Give a bounding box for every artifact (platelet-like body, stain precipitate, or debris).
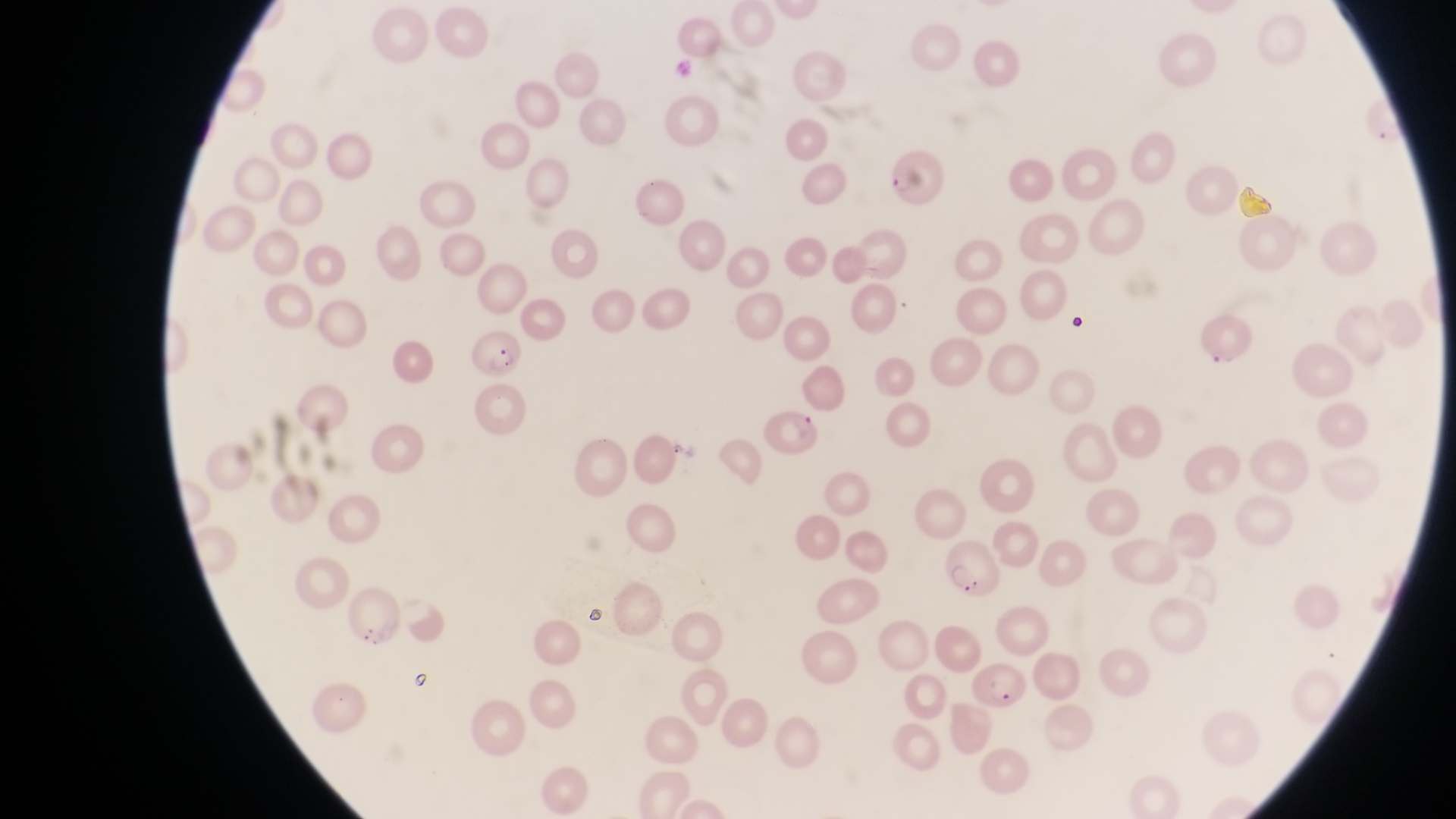
Approximate bounding boxes as [left, top, right, bottom] in pixels.
Artifacts (platelet-like body, stain precipitate, or debris): [1237, 179, 1280, 231], [1068, 312, 1091, 336], [582, 602, 606, 626], [409, 668, 441, 695].

magnification = 1000x
trophozoite locations = approximate bounding boxes as [left, top, right, bottom] in pixels: [667, 435, 694, 465]
parasitised red blood cell locations = approximate bounding boxes as [left, top, right, bottom] in pixels: [888, 151, 951, 212], [1199, 309, 1252, 370], [468, 330, 524, 379], [767, 404, 819, 453], [948, 544, 998, 596], [970, 657, 1028, 712]
image size = 1456×819 pixels
country = Uganda
field of view = single
preparation = thin blood film
capture = smartphone photograph through the eyepiece of an Olympus CX-23 microscope